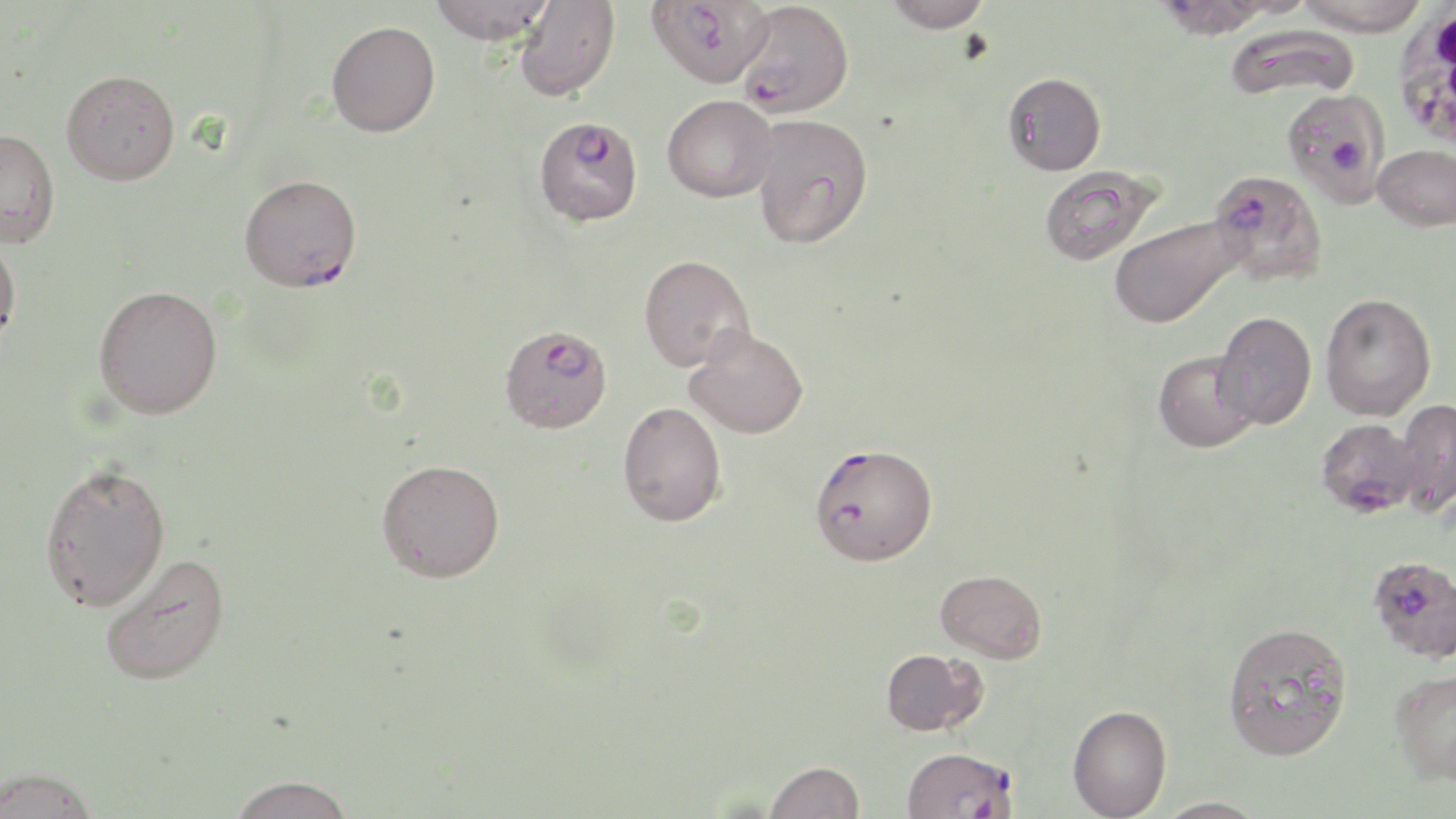

slide-level diagnosis = Plasmodium falciparum
modality = optical microscopy
image size = 1456×819 pixels
Plasmodium falciparum-infected red blood cell locations = approximate bounding boxes as (x1,y1)-(x2,y2) corner pairs in pixels: (646,0)-(773,88), (735,1)-(854,118), (1281,87)-(1390,206), (536,122)-(643,223), (1207,169)-(1327,287), (239,174)-(362,292), (503,330)-(610,434), (1316,417)-(1424,517), (811,451)-(944,570), (1369,555)-(1456,661), (902,746)-(1019,818)
stain = May-Grünwald-Giemsa
magnification = 1000x
preparation = thin blood smear
uninfected red blood cell locations = approximate bounding boxes as (x1,y1)-(x2,y2) corner pairs in pixels: (429,0)-(555,44), (883,0)-(993,33), (1295,0)-(1431,36), (514,1)-(620,102), (326,20)-(440,137), (1223,24)-(1361,103), (61,69)-(180,185), (1002,72)-(1106,176), (662,94)-(778,202), (750,113)-(873,249), (0,129)-(60,248), (1373,144)-(1456,230), (1039,166)-(1161,265), (1108,215)-(1243,328), (0,229)-(22,351), (638,254)-(755,372), (93,284)-(223,419), (1320,292)-(1436,421), (1213,311)-(1317,429), (684,325)-(809,438), (1153,350)-(1260,452), (1395,398)-(1456,518), (618,401)-(727,526), (377,458)-(505,582), (39,461)-(171,611), (97,551)-(230,686), (936,569)-(1047,663), (1221,621)-(1353,761), (880,648)-(987,736), (1389,668)-(1456,784), (1067,704)-(1172,818), (764,760)-(865,819), (0,767)-(101,819), (227,775)-(355,819), (1154,796)-(1271,819)
field of view = one of a larger specimen
white blood cell locations = approximate bounding boxes as (x1,y1)-(x2,y2) corner pairs in pixels: (1392,4)-(1456,153)